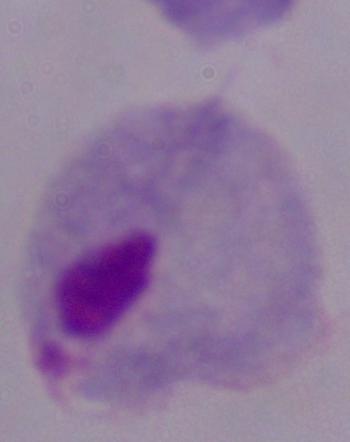
identification = trichomonad
modality = photomicrograph
magnification = 1000x